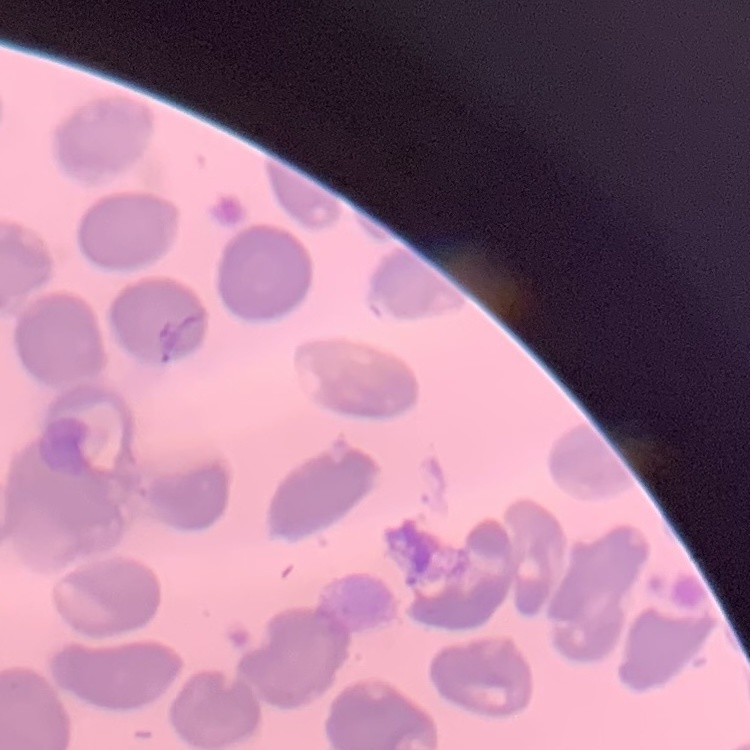
The red blood cells show no rouleaux formation. Stained with either Field's or Giemsa. Square crop of a larger photomicrograph. Thin blood film.